State which cell type is depicted.
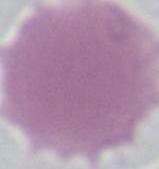
This is an erythrocyte.

Summary:
  - Modality: micrograph
  - Magnification: 1000x